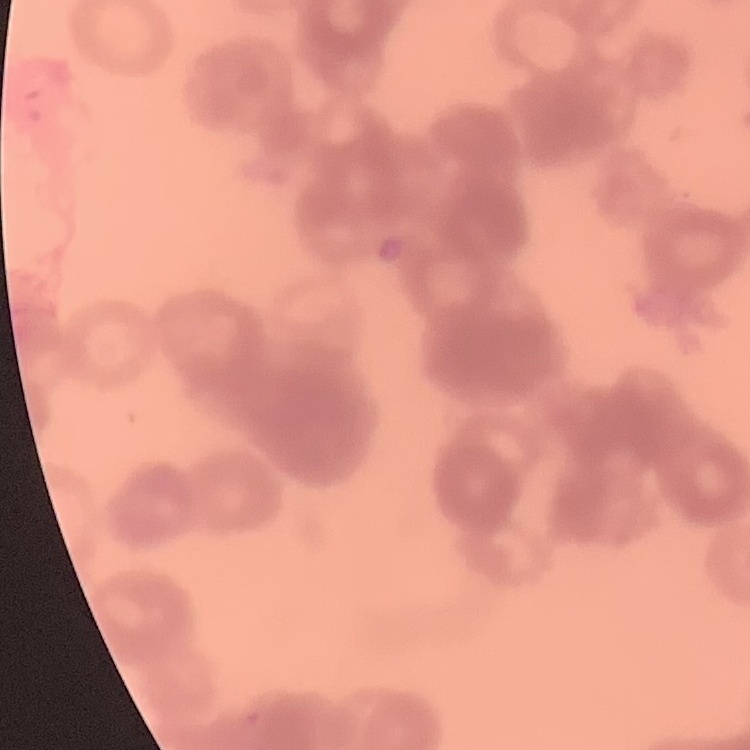
erythrocyte morphology = rouleaux formation
image type = one tile cut from a larger photomicrograph
preparation = thin blood film
stain = Field's or Giemsa